Locate every Plasmodium parasite.
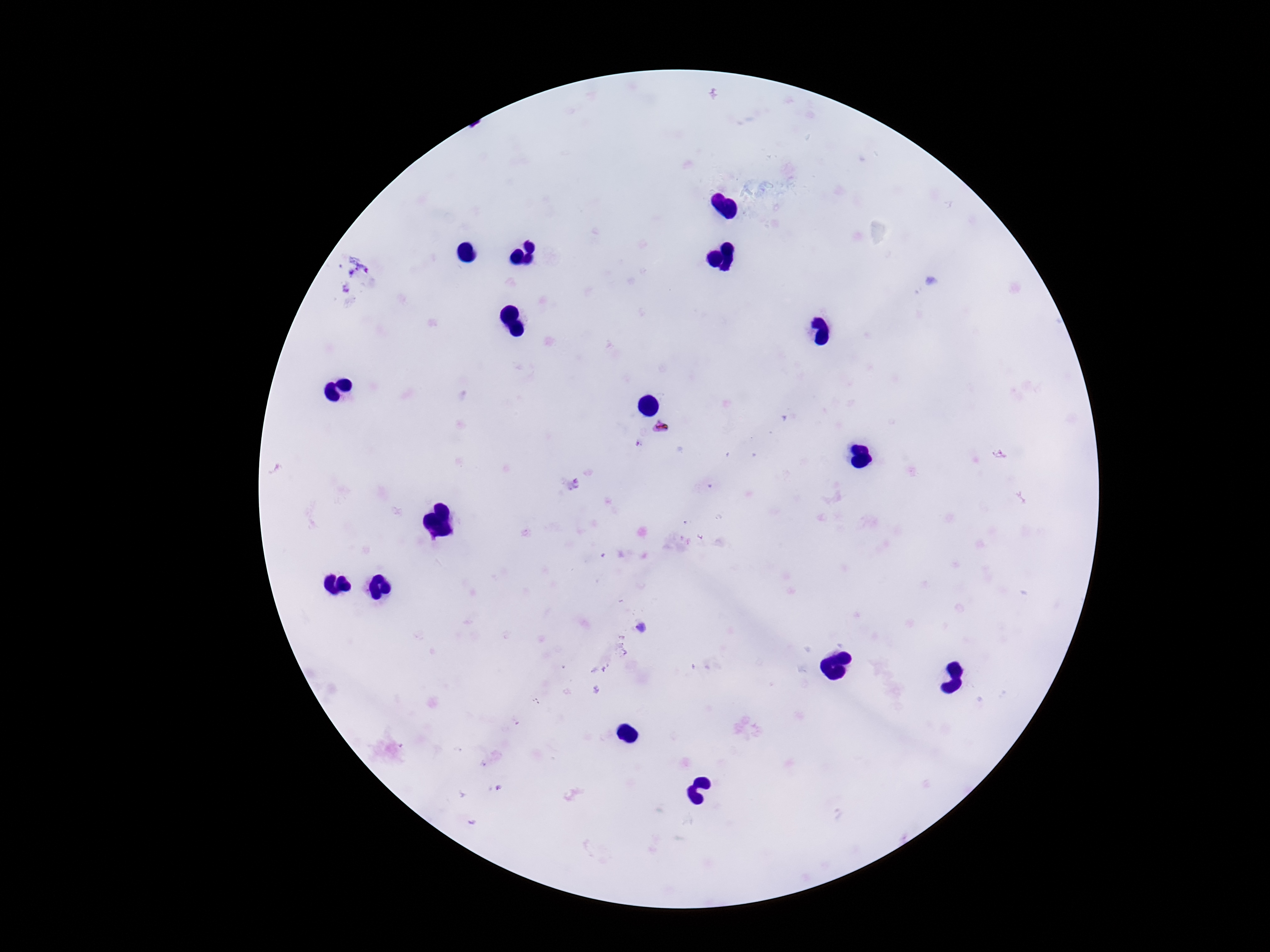
Approximate object centers, in pixels from the top-left corner.
Plasmodium parasites: (x=659, y=427).

Single field of view. Giemsa-stained preparation. Patient malaria status: infected. Photographed through the microscope eyepiece with a smartphone camera. Image is 1270×952 pixels. 100x magnification. Thick peripheral-blood smear.